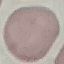
Summary:
  - Result: negative for malaria parasites
  - Capture: smartphone camera at the microscope eyepiece
  - Image type: automatically extracted cell patch, resized to 64 × 64 pixels
  - Stain: Giemsa
  - Preparation: thin blood smear